Identify the parasite.
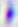

This is Toxoplasma gondii.

modality: photomicrograph
magnification: 400x